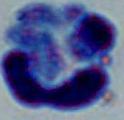

A white blood cell is seen. Micrograph. 1000x magnification.